Report the malaria status of this cell.
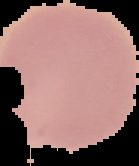
It is uninfected.

{
  "image_type": "cell region segmented out of the field of view; surrounding area masked to black",
  "image_size": "139×166 pixels",
  "preparation": "thin blood smear"
}